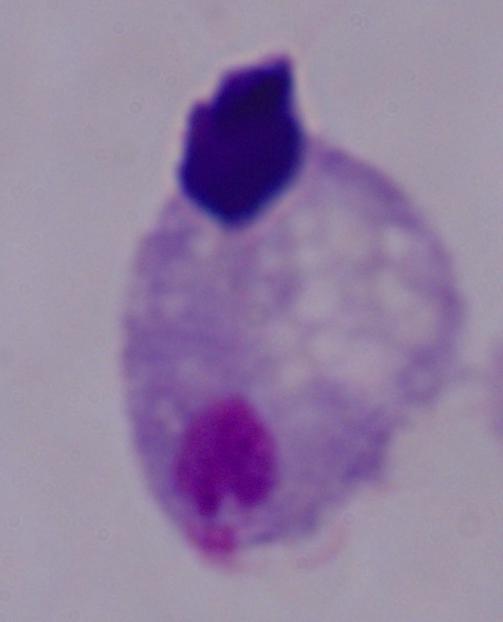
modality = photomicrograph
identification = trichomonad
magnification = 1000x